Comment on the morphology of the erythrocytes.
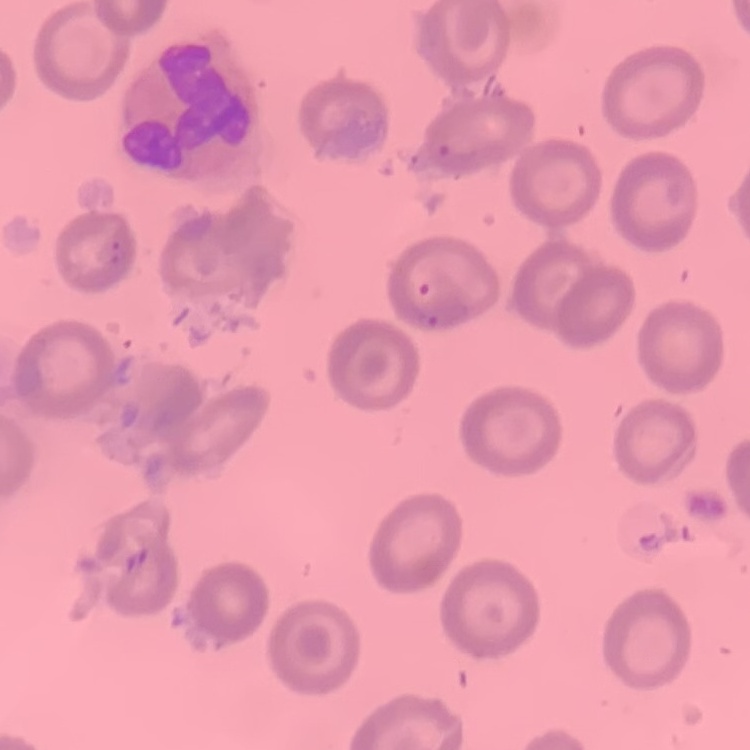
They show no rouleaux formation.

Summary:
  - Image type: one tile cut from a larger photomicrograph
  - Preparation: thin blood smear
  - Stain: Field's or Giemsa